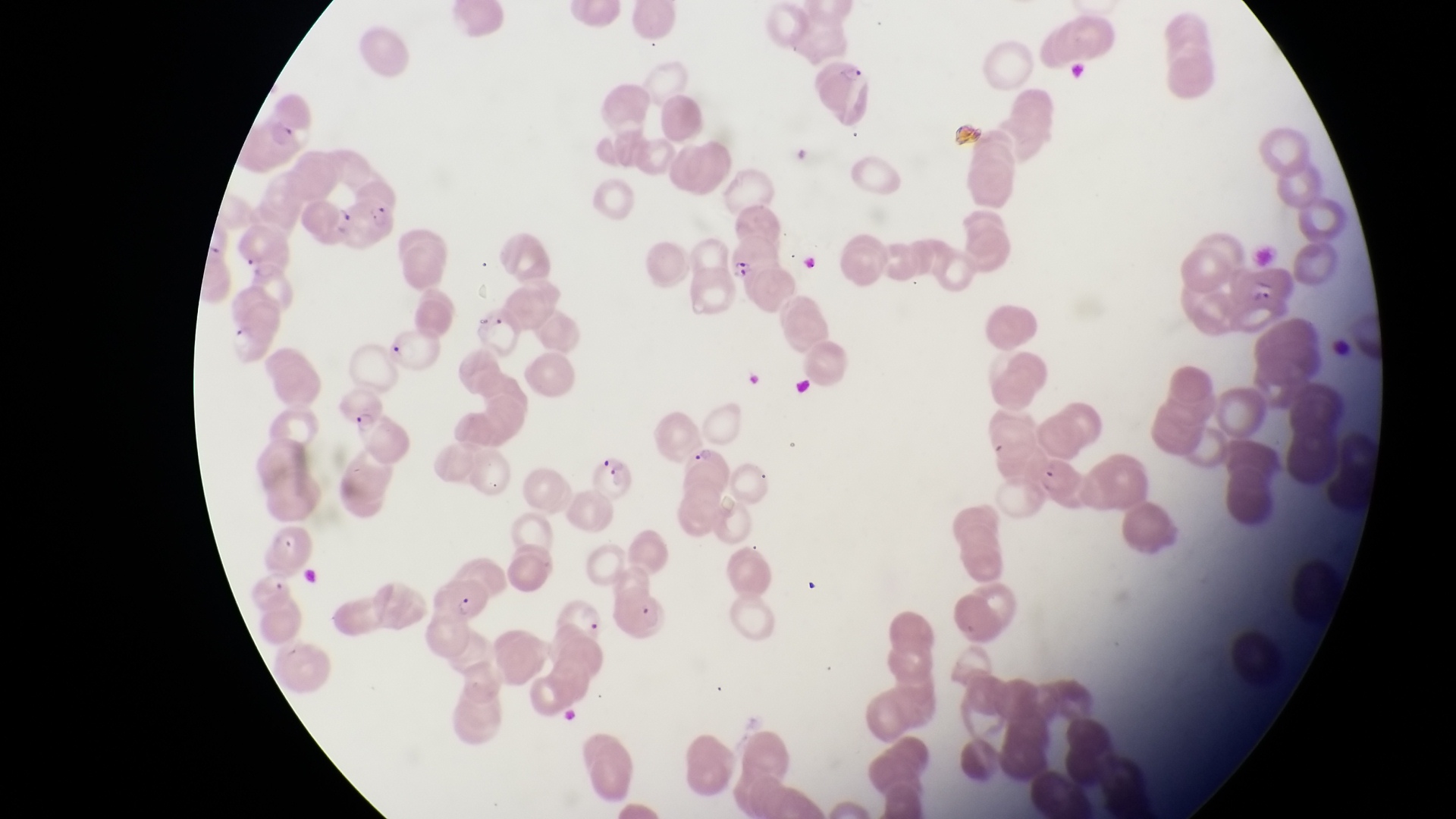

Approximate bounding boxes as [left, top, right, bottom] in pixels.
Summary:
  - Parasitised red blood cell locations: [338, 198, 396, 250], [733, 227, 783, 285], [334, 389, 387, 442], [686, 439, 732, 502], [587, 444, 634, 502], [435, 573, 490, 625], [560, 595, 610, 645]
  - Artifact (platelet-like body, stain precipitate, or debris) locations: [792, 139, 829, 189], [475, 306, 498, 338], [384, 336, 410, 365]
  - Magnification: 1000x
  - Capture: smartphone photograph through the eyepiece of an Olympus CX-23 microscope
  - Field of view: single
  - Image size: 1456×819 pixels
  - Preparation: thin blood smear
  - Country: Uganda